Locate and identify every blood parasite.
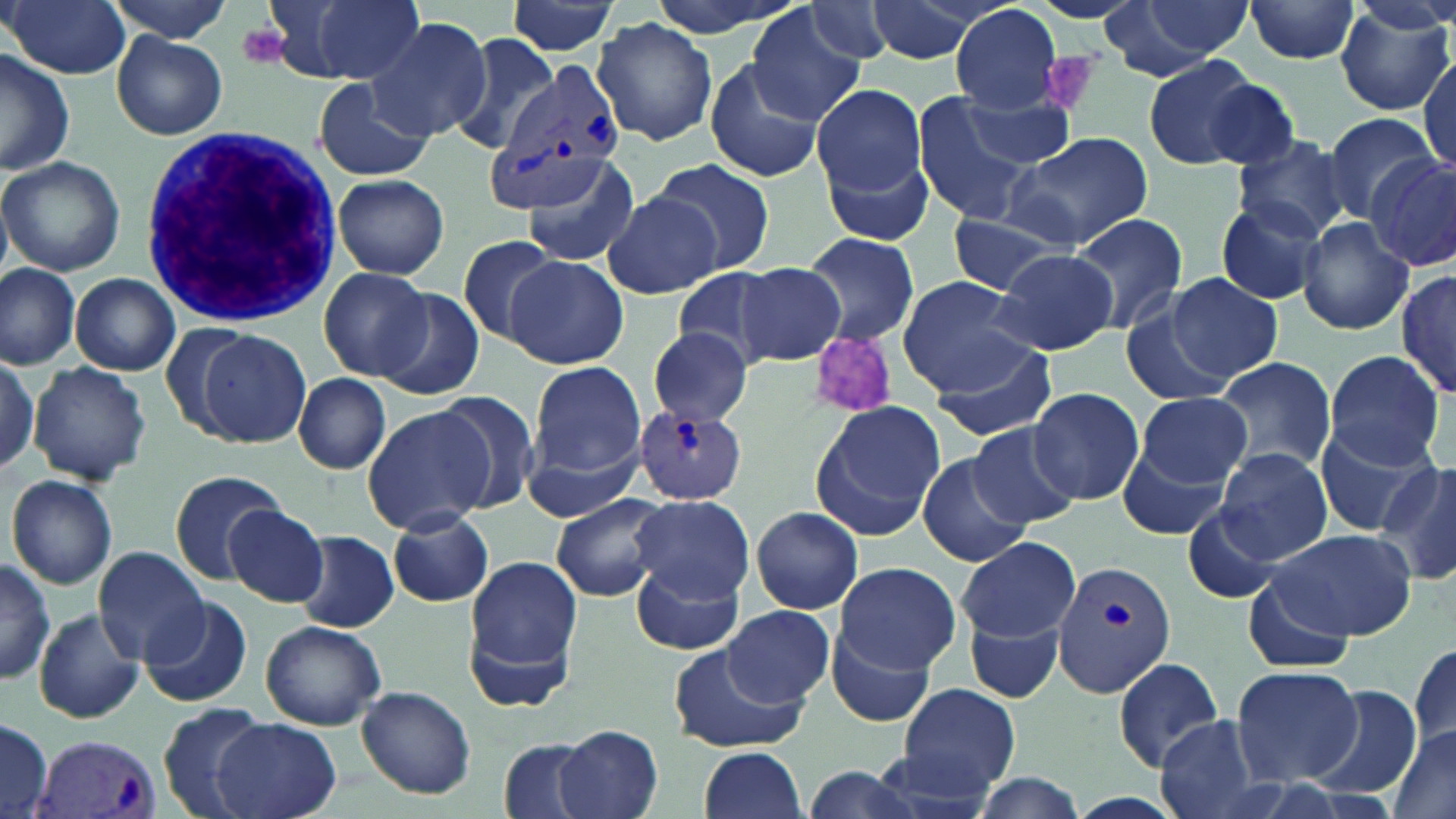
Approximate bounding boxes as named x1/y1/x2/y2 corners in pixels.
Plasmodium vivax-infected red blood cells: (x1=487, y1=70, x2=622, y2=213), (x1=633, y1=405, x2=749, y2=504), (x1=1050, y1=558, x2=1176, y2=695), (x1=36, y1=733, x2=166, y2=819).
No Plasmodium falciparum, Plasmodium ovale, Plasmodium malariae, Babesia divergens, or Trypanosoma brucei observed.

Platelet locations: (x1=238, y1=24, x2=291, y2=69), (x1=1041, y1=49, x2=1102, y2=112), (x1=806, y1=330, x2=901, y2=420). Uninfected red blood cell locations: (x1=4, y1=0, x2=131, y2=80), (x1=106, y1=0, x2=231, y2=44), (x1=279, y1=0, x2=430, y2=86), (x1=645, y1=0, x2=805, y2=38), (x1=861, y1=0, x2=986, y2=64), (x1=1103, y1=0, x2=1247, y2=77), (x1=1244, y1=0, x2=1361, y2=65), (x1=506, y1=1, x2=619, y2=57), (x1=1336, y1=1, x2=1454, y2=116), (x1=799, y1=2, x2=900, y2=65), (x1=951, y1=4, x2=1064, y2=114), (x1=747, y1=8, x2=867, y2=127), (x1=592, y1=17, x2=721, y2=146), (x1=366, y1=18, x2=492, y2=140), (x1=449, y1=30, x2=559, y2=156), (x1=113, y1=31, x2=227, y2=140), (x1=0, y1=48, x2=77, y2=176), (x1=1417, y1=55, x2=1455, y2=180), (x1=1141, y1=56, x2=1267, y2=171), (x1=703, y1=59, x2=825, y2=183), (x1=1194, y1=75, x2=1301, y2=172), (x1=311, y1=78, x2=434, y2=182), (x1=811, y1=81, x2=930, y2=211), (x1=959, y1=90, x2=1078, y2=169), (x1=914, y1=96, x2=1039, y2=228), (x1=1320, y1=112, x2=1441, y2=219), (x1=1008, y1=132, x2=1153, y2=249), (x1=1230, y1=134, x2=1352, y2=242), (x1=1367, y1=152, x2=1454, y2=270), (x1=0, y1=155, x2=126, y2=277), (x1=520, y1=156, x2=645, y2=271), (x1=654, y1=156, x2=776, y2=275), (x1=332, y1=174, x2=449, y2=279), (x1=602, y1=190, x2=724, y2=300), (x1=1213, y1=199, x2=1329, y2=305), (x1=1069, y1=213, x2=1186, y2=333), (x1=945, y1=215, x2=1069, y2=294), (x1=1295, y1=217, x2=1414, y2=335), (x1=801, y1=232, x2=919, y2=347), (x1=455, y1=234, x2=563, y2=346), (x1=990, y1=248, x2=1121, y2=355), (x1=503, y1=254, x2=628, y2=370), (x1=733, y1=262, x2=846, y2=368), (x1=0, y1=263, x2=81, y2=369), (x1=318, y1=266, x2=434, y2=382), (x1=675, y1=268, x2=779, y2=368), (x1=1397, y1=268, x2=1455, y2=400), (x1=1166, y1=272, x2=1283, y2=383), (x1=71, y1=273, x2=180, y2=376), (x1=897, y1=276, x2=1036, y2=393), (x1=376, y1=289, x2=485, y2=400), (x1=1120, y1=308, x2=1237, y2=407), (x1=195, y1=329, x2=312, y2=448), (x1=648, y1=330, x2=755, y2=425), (x1=927, y1=335, x2=1060, y2=443), (x1=1325, y1=349, x2=1447, y2=466), (x1=0, y1=353, x2=40, y2=474), (x1=1210, y1=356, x2=1339, y2=474), (x1=525, y1=359, x2=649, y2=493), (x1=27, y1=360, x2=151, y2=486), (x1=293, y1=373, x2=391, y2=474), (x1=1027, y1=386, x2=1143, y2=505), (x1=1138, y1=391, x2=1253, y2=487), (x1=433, y1=393, x2=541, y2=513), (x1=810, y1=401, x2=947, y2=537), (x1=362, y1=404, x2=493, y2=534), (x1=1316, y1=420, x2=1437, y2=537), (x1=967, y1=423, x2=1080, y2=529), (x1=1115, y1=437, x2=1233, y2=542), (x1=1215, y1=446, x2=1335, y2=565), (x1=919, y1=452, x2=1031, y2=569), (x1=1378, y1=456, x2=1456, y2=585), (x1=170, y1=471, x2=292, y2=587), (x1=6, y1=474, x2=118, y2=590), (x1=551, y1=492, x2=669, y2=601), (x1=631, y1=493, x2=754, y2=601), (x1=1178, y1=505, x2=1281, y2=606), (x1=224, y1=506, x2=329, y2=607), (x1=750, y1=506, x2=865, y2=615), (x1=387, y1=509, x2=495, y2=606), (x1=1264, y1=528, x2=1412, y2=642), (x1=293, y1=531, x2=400, y2=632), (x1=957, y1=537, x2=1081, y2=642), (x1=92, y1=546, x2=211, y2=664), (x1=464, y1=551, x2=585, y2=692), (x1=0, y1=556, x2=55, y2=685), (x1=631, y1=559, x2=744, y2=656), (x1=835, y1=561, x2=961, y2=675), (x1=1241, y1=577, x2=1356, y2=675), (x1=140, y1=596, x2=253, y2=709), (x1=723, y1=605, x2=835, y2=708), (x1=34, y1=609, x2=145, y2=725), (x1=967, y1=618, x2=1064, y2=702), (x1=260, y1=619, x2=387, y2=730), (x1=827, y1=619, x2=939, y2=728), (x1=1408, y1=640, x2=1456, y2=753), (x1=667, y1=646, x2=805, y2=754), (x1=1111, y1=656, x2=1226, y2=771), (x1=1232, y1=663, x2=1362, y2=787), (x1=897, y1=683, x2=1020, y2=795), (x1=355, y1=685, x2=477, y2=799), (x1=1308, y1=687, x2=1418, y2=801), (x1=155, y1=703, x2=267, y2=819), (x1=1342, y1=705, x2=1443, y2=817), (x1=1154, y1=713, x2=1270, y2=819), (x1=212, y1=717, x2=342, y2=819), (x1=0, y1=719, x2=54, y2=817), (x1=556, y1=723, x2=664, y2=819), (x1=1384, y1=724, x2=1456, y2=817), (x1=498, y1=738, x2=602, y2=819), (x1=698, y1=747, x2=808, y2=819), (x1=969, y1=771, x2=1091, y2=819). White blood cell locations: (x1=133, y1=123, x2=347, y2=327). Slide-level diagnosis: Plasmodium vivax. Light microscopy. One field of a larger specimen. 1000x magnification. May-Grünwald-Giemsa-stained preparation. Image is 1456×819 pixels. Thin blood film.